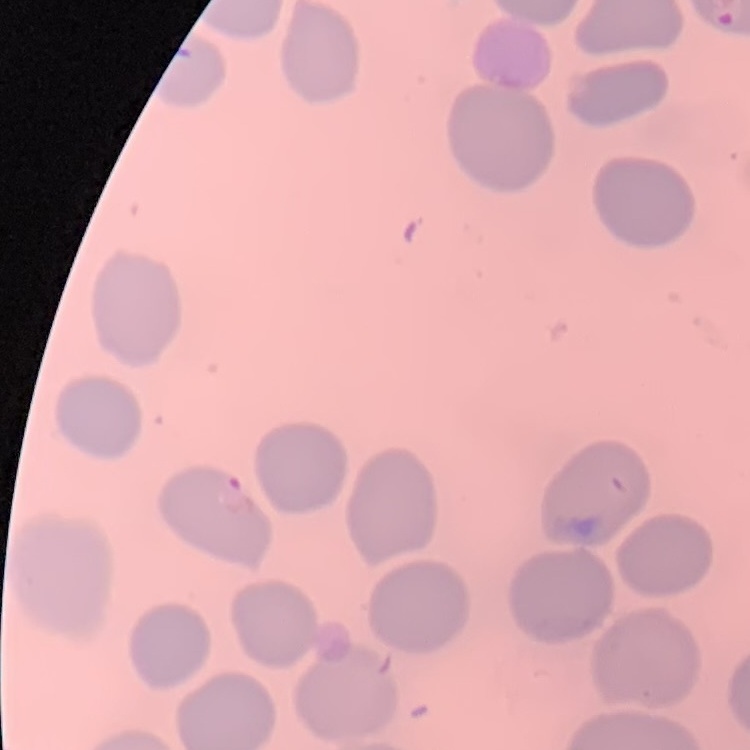

{
  "red_blood_cell_morphology": "no rouleaux formation",
  "stain": "Field's or Giemsa",
  "preparation": "thin blood smear",
  "image_type": "one tile cut from a larger photomicrograph"
}